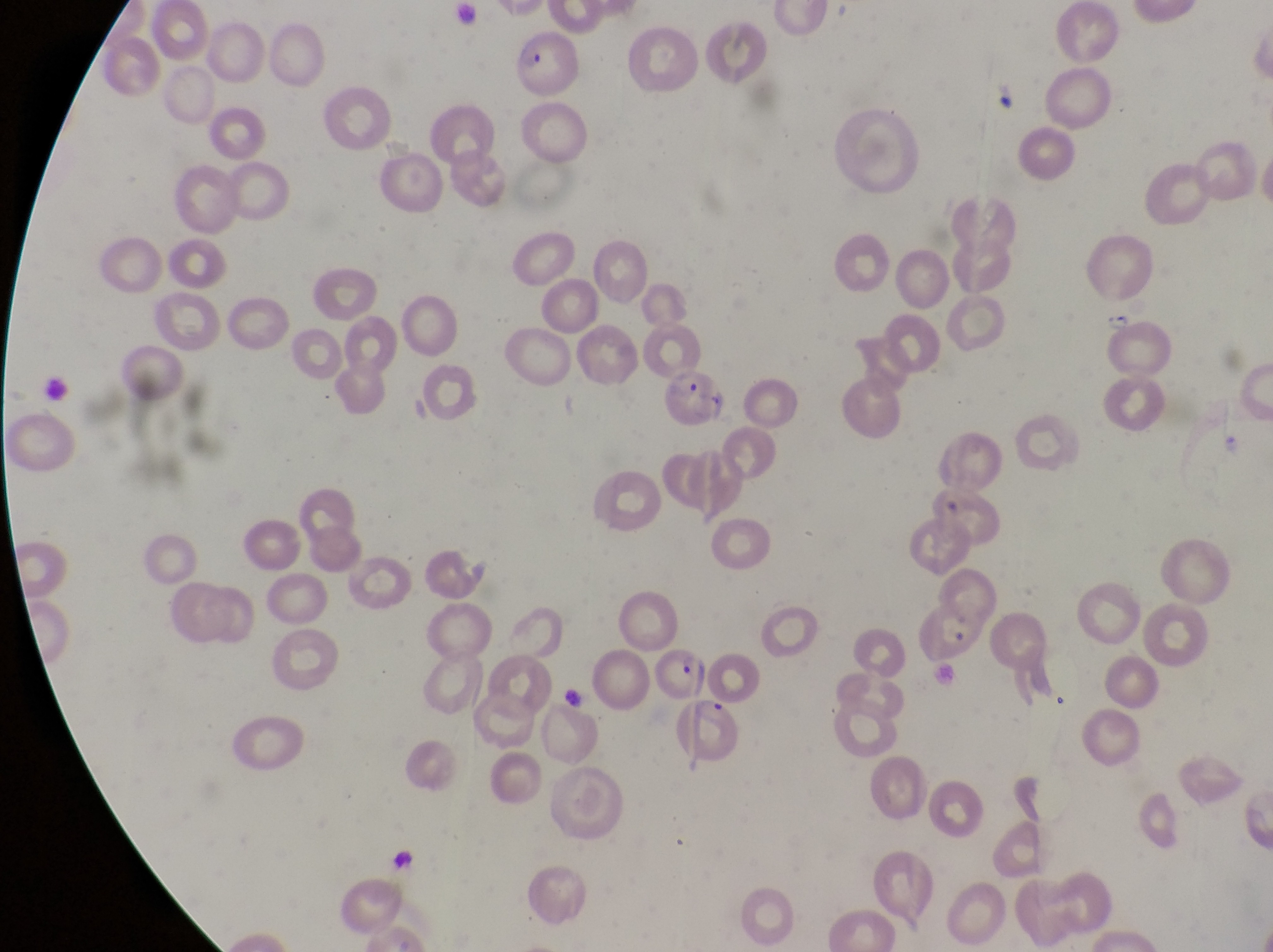

Approximate bounding boxes as [left, top, right, bottom] in pixels. Trophozoite locations: [1099, 305, 1134, 337]. Parasitised red blood cell locations: [514, 34, 576, 94], [664, 372, 726, 429], [911, 602, 978, 664], [652, 639, 705, 696], [679, 697, 749, 771]. Sample from Uganda. At a magnification of 1000x. One field of view. Photographed through the eyepiece of an Olympus CX-23 microscope with a smartphone camera. Image is 1273×952 pixels. Thin blood smear.